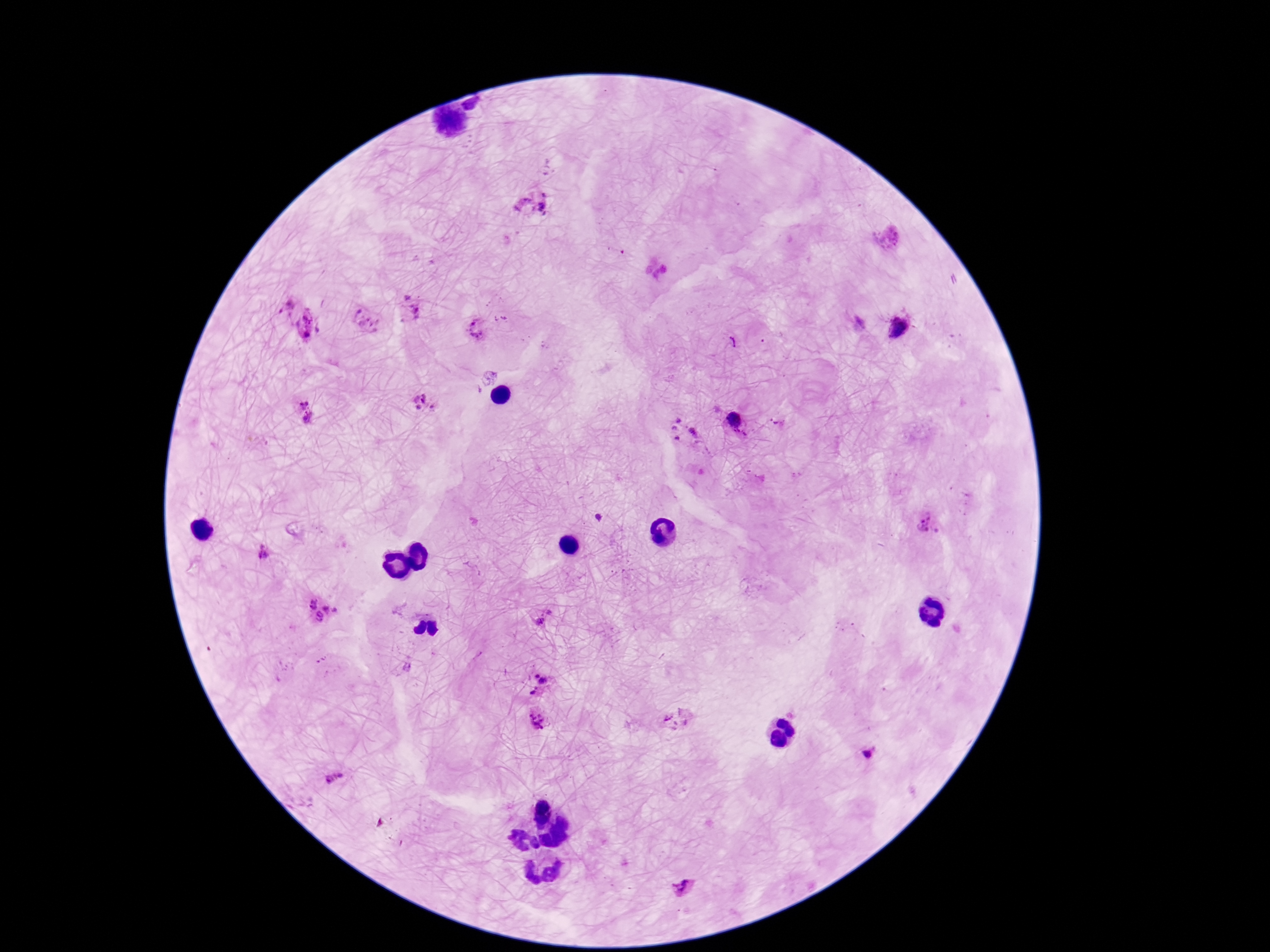

field of view = one from this slide
capture = smartphone camera through the microscope eyepiece
stain = Giemsa
preparation = thick blood film
Plasmodium parasite locations = approximate centers as (x, y) in pixels: (533, 203), (283, 299), (410, 309), (367, 321), (308, 326), (901, 329), (477, 330), (423, 404), (304, 412), (736, 422), (684, 433), (929, 524), (262, 552), (319, 609), (544, 618), (537, 684), (537, 719), (872, 755), (333, 778), (683, 887)
image size = 1270×952 pixels
patient malaria status = infected
magnification = 100x